Classify this cell by malaria status.
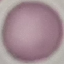
Uninfected.

image type = cell patch, automatically extracted from a larger field of view and resized to 64 × 64 pixels
capture = smartphone camera at the microscope eyepiece
stain = Giemsa
preparation = thin smear